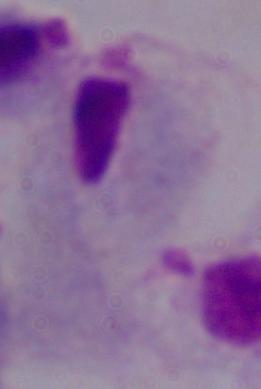

Captured at 1000x magnification. Photomicrograph. A trichomonad is shown.